Locate every Plasmodium malariae-infected red blood cell.
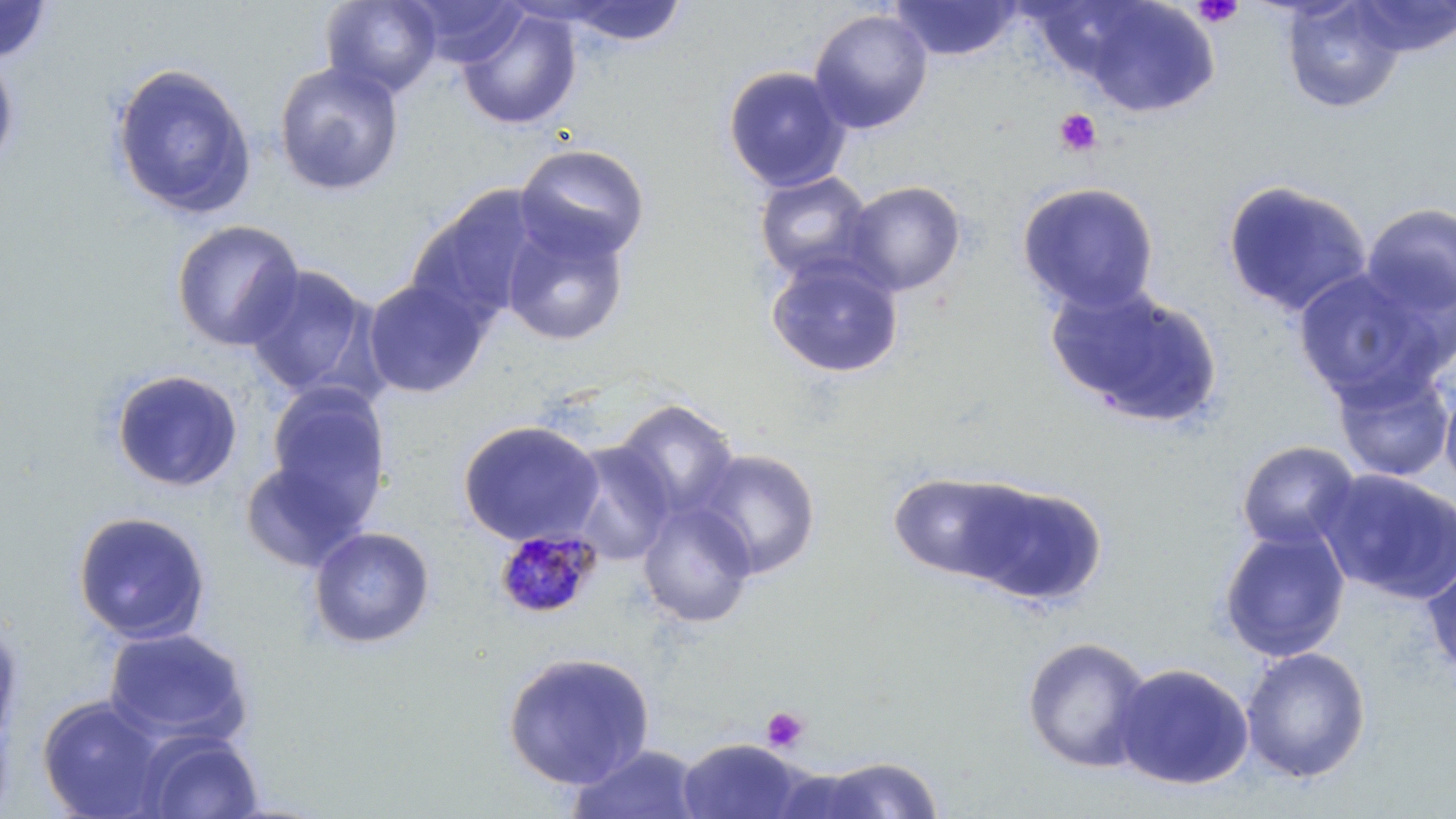

Approximate bounding boxes as (x1,y1)-(x2,y2) corner pairs in pixels.
Plasmodium malariae-infected red blood cells: (492,528)-(604,620).

Platelet locations: (1192,0)-(1244,29), (1054,108)-(1101,157), (761,706)-(809,752). Uninfected red blood cell locations: (0,0)-(55,65), (321,0)-(443,99), (406,0)-(529,67), (889,0)-(1024,61), (1280,0)-(1406,114), (1350,0)-(1456,56), (555,1)-(689,48), (1077,1)-(1219,118), (457,8)-(582,131), (808,8)-(933,134), (0,48)-(19,175), (109,61)-(258,220), (273,61)-(406,197), (722,65)-(851,192), (514,142)-(650,265), (753,170)-(875,283), (1221,179)-(1373,318), (842,180)-(966,296), (1016,181)-(1160,314), (407,186)-(544,326), (1360,202)-(1456,323), (500,218)-(630,346), (171,219)-(306,352), (765,253)-(905,379), (242,263)-(376,398), (1293,267)-(1449,406), (361,277)-(491,398), (1046,282)-(1223,429), (1332,364)-(1455,482), (110,368)-(243,493), (1439,376)-(1456,497), (266,382)-(391,519), (613,399)-(739,519), (457,419)-(606,547), (563,440)-(677,565), (1236,440)-(1361,551), (691,448)-(822,580), (238,455)-(371,574), (1317,468)-(1456,604), (887,470)-(1033,581), (960,481)-(1108,607), (637,500)-(757,628), (72,510)-(212,645), (1217,525)-(1351,663), (307,526)-(436,649), (1421,554)-(1456,679), (0,612)-(26,751), (102,626)-(253,747), (1021,636)-(1154,773), (1239,646)-(1372,783), (501,651)-(656,791), (1112,661)-(1254,791), (37,694)-(171,818), (136,731)-(265,819), (676,737)-(810,819), (566,744)-(704,819), (810,755)-(945,817), (766,767)-(890,817). Slide-level diagnosis: Plasmodium malariae. Captured at 1000x magnification. Image is 1456×819 pixels. Light microscopy. Single field of view. May-Grünwald-Giemsa-stained preparation. Thin blood film.